Give the extent of all uninfected red blood cells.
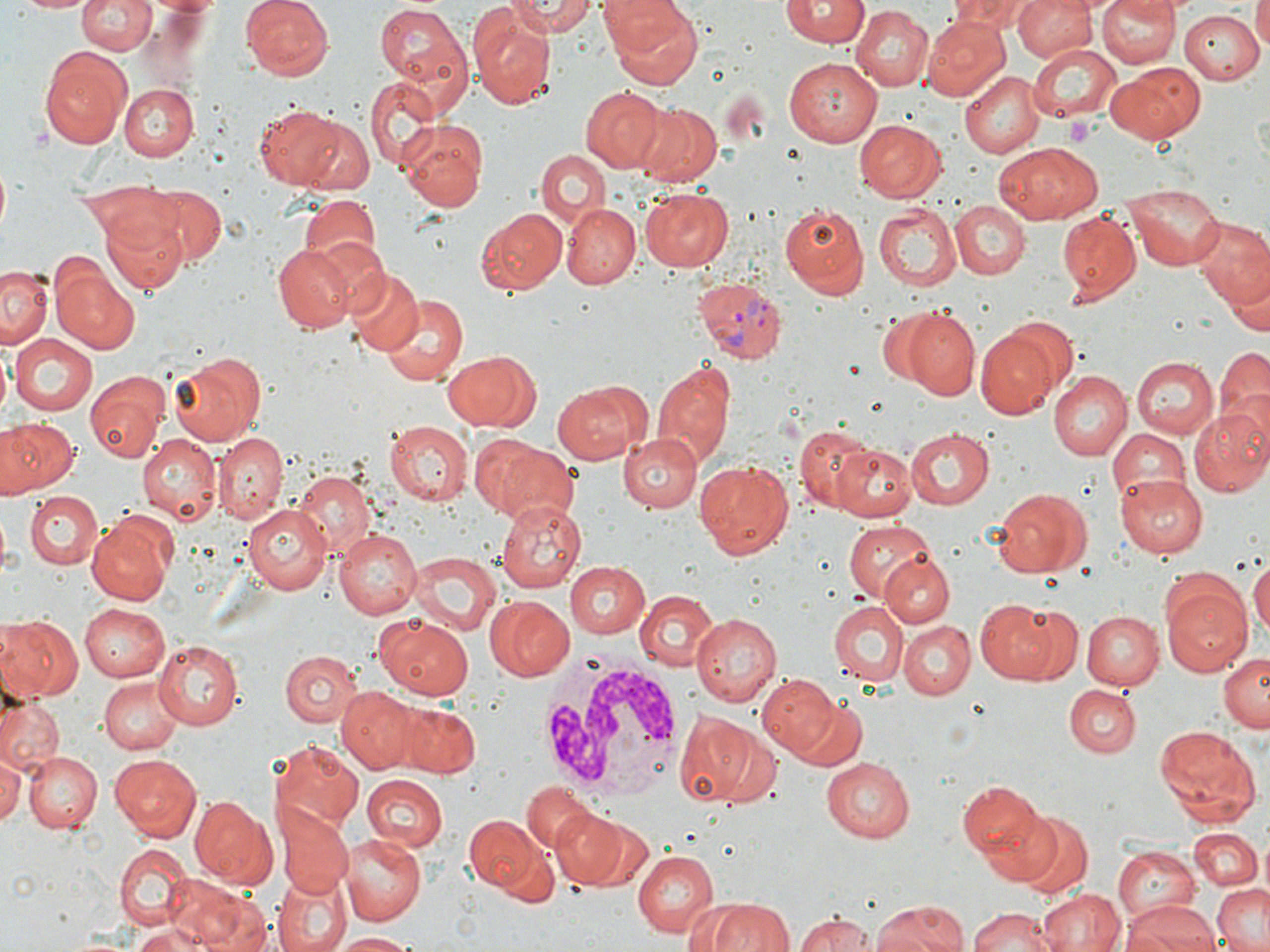

Approximate bounding boxes as [x1, y1, x2, y2] in pixels.
Uninfected red blood cells: [13, 0, 93, 15], [77, 0, 156, 57], [242, 0, 333, 81], [502, 0, 598, 38], [604, 0, 705, 88], [781, 0, 867, 48], [948, 0, 1036, 34], [1012, 0, 1097, 64], [1095, 0, 1177, 69], [1253, 0, 1270, 52], [374, 1, 472, 95], [1096, 3, 1258, 75], [851, 7, 933, 92], [472, 9, 557, 109], [1179, 9, 1265, 84], [922, 16, 1009, 100], [1026, 43, 1122, 122], [39, 44, 133, 148], [784, 56, 883, 146], [1108, 63, 1205, 143], [960, 71, 1043, 159], [365, 77, 440, 170], [115, 82, 197, 160], [580, 86, 665, 171], [251, 102, 359, 190], [635, 103, 719, 186], [296, 117, 375, 197], [396, 118, 489, 210], [855, 119, 947, 202], [994, 143, 1098, 225], [535, 154, 607, 234], [135, 181, 226, 269], [1122, 183, 1224, 272], [640, 188, 734, 271], [296, 192, 382, 281], [949, 201, 1030, 279], [776, 202, 869, 298], [872, 203, 959, 291], [563, 205, 640, 288], [475, 207, 568, 296], [104, 211, 187, 296], [1057, 211, 1142, 306], [1192, 217, 1270, 311], [270, 244, 356, 331], [0, 267, 51, 348], [54, 267, 138, 354], [345, 269, 423, 355], [1229, 276, 1270, 336], [379, 294, 468, 386], [892, 307, 979, 399], [978, 330, 1061, 419], [10, 333, 97, 416], [1215, 347, 1269, 431], [443, 348, 541, 432], [168, 351, 268, 445], [1134, 357, 1218, 439], [652, 359, 736, 468], [1047, 369, 1132, 460], [84, 372, 168, 461], [553, 383, 640, 464], [1187, 405, 1270, 497], [0, 417, 78, 495], [386, 422, 472, 506], [793, 425, 879, 510], [904, 427, 994, 509], [1105, 429, 1192, 507], [617, 430, 704, 514], [470, 433, 554, 515], [138, 434, 220, 525], [215, 434, 285, 522], [834, 439, 919, 520], [494, 443, 578, 525], [694, 459, 794, 559], [292, 470, 373, 553], [1116, 475, 1207, 557], [992, 488, 1091, 578], [22, 490, 100, 568], [499, 497, 589, 593], [245, 500, 333, 592], [87, 514, 175, 605], [840, 518, 936, 606], [334, 526, 421, 619], [407, 551, 500, 634], [881, 553, 953, 628], [1249, 558, 1270, 639], [564, 559, 651, 638], [1160, 572, 1253, 676], [634, 590, 720, 673], [485, 595, 575, 681], [829, 598, 908, 685], [978, 600, 1056, 682], [78, 604, 170, 683], [1015, 607, 1083, 682], [1080, 609, 1162, 691], [691, 612, 782, 705], [377, 614, 476, 700], [0, 617, 81, 701], [900, 620, 975, 699], [154, 641, 244, 730], [280, 650, 363, 729], [1219, 653, 1269, 732], [757, 672, 843, 758], [98, 678, 184, 754], [1064, 683, 1141, 760], [337, 685, 417, 773], [1, 696, 64, 771], [791, 697, 868, 770], [398, 703, 482, 776], [673, 706, 777, 806], [1153, 724, 1261, 827], [273, 740, 367, 831], [24, 753, 102, 831], [109, 753, 204, 840], [0, 755, 22, 824], [821, 756, 914, 841], [361, 774, 449, 853], [959, 781, 1047, 860], [521, 784, 594, 853], [188, 794, 276, 886], [275, 802, 355, 896], [978, 806, 1066, 887], [550, 808, 629, 887], [464, 814, 543, 893], [1011, 814, 1093, 896], [1189, 830, 1263, 892], [341, 831, 429, 925], [115, 844, 190, 927], [1112, 845, 1203, 927], [631, 848, 719, 936], [275, 873, 349, 952], [164, 876, 257, 950], [1209, 881, 1270, 952], [1040, 888, 1126, 952], [703, 895, 795, 952], [194, 896, 275, 952], [869, 900, 972, 952], [1123, 903, 1220, 952], [966, 907, 1057, 952], [794, 911, 880, 951], [129, 924, 208, 952], [330, 932, 424, 950].

Platelet locations: [1064, 116, 1097, 147]. Plasmodium vivax-infected red blood cell locations: [695, 275, 789, 362]. White blood cell locations: [538, 651, 685, 798]. Slide-level diagnosis: Plasmodium vivax. Image is 1270×952 pixels. Thin blood smear. One field of a larger specimen. May-Grünwald-Giemsa stain. Optical microscopy. Captured at 1000x magnification.